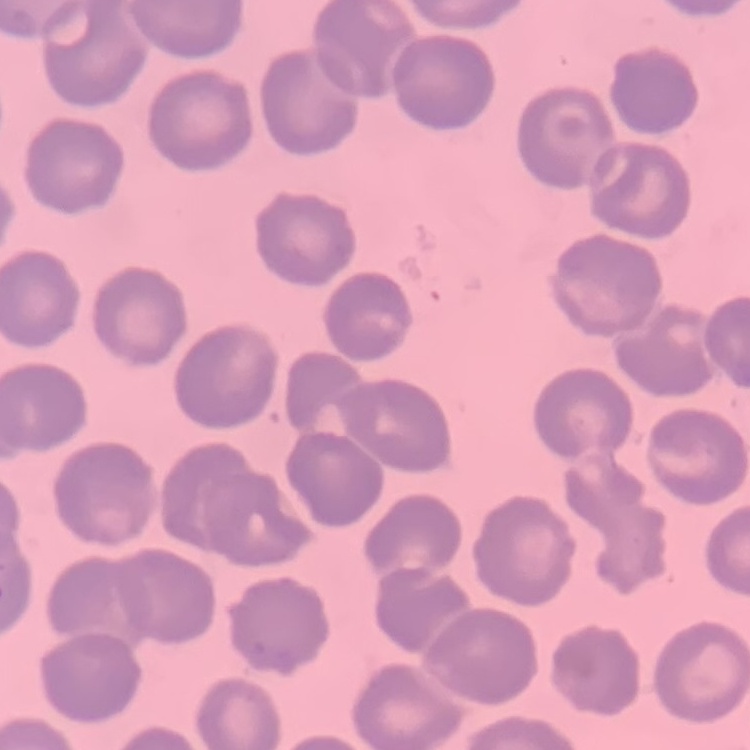
Summary:
  - Red blood cell morphology: no rouleaux formation
  - Image type: square crop of a larger photomicrograph
  - Stain: Field's or Giemsa
  - Preparation: thin peripheral smear